Report the malaria status of this cell.
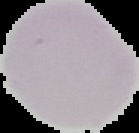

Uninfected.

Summary:
  - Image type: segmented cell region with the area outside set to black
  - Preparation: thin blood film
  - Image size: 139×133 pixels